Identify the cell.
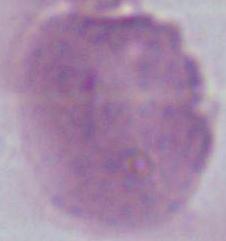
An erythrocyte.

Summary:
  - Modality: photomicrograph
  - Magnification: 1000x